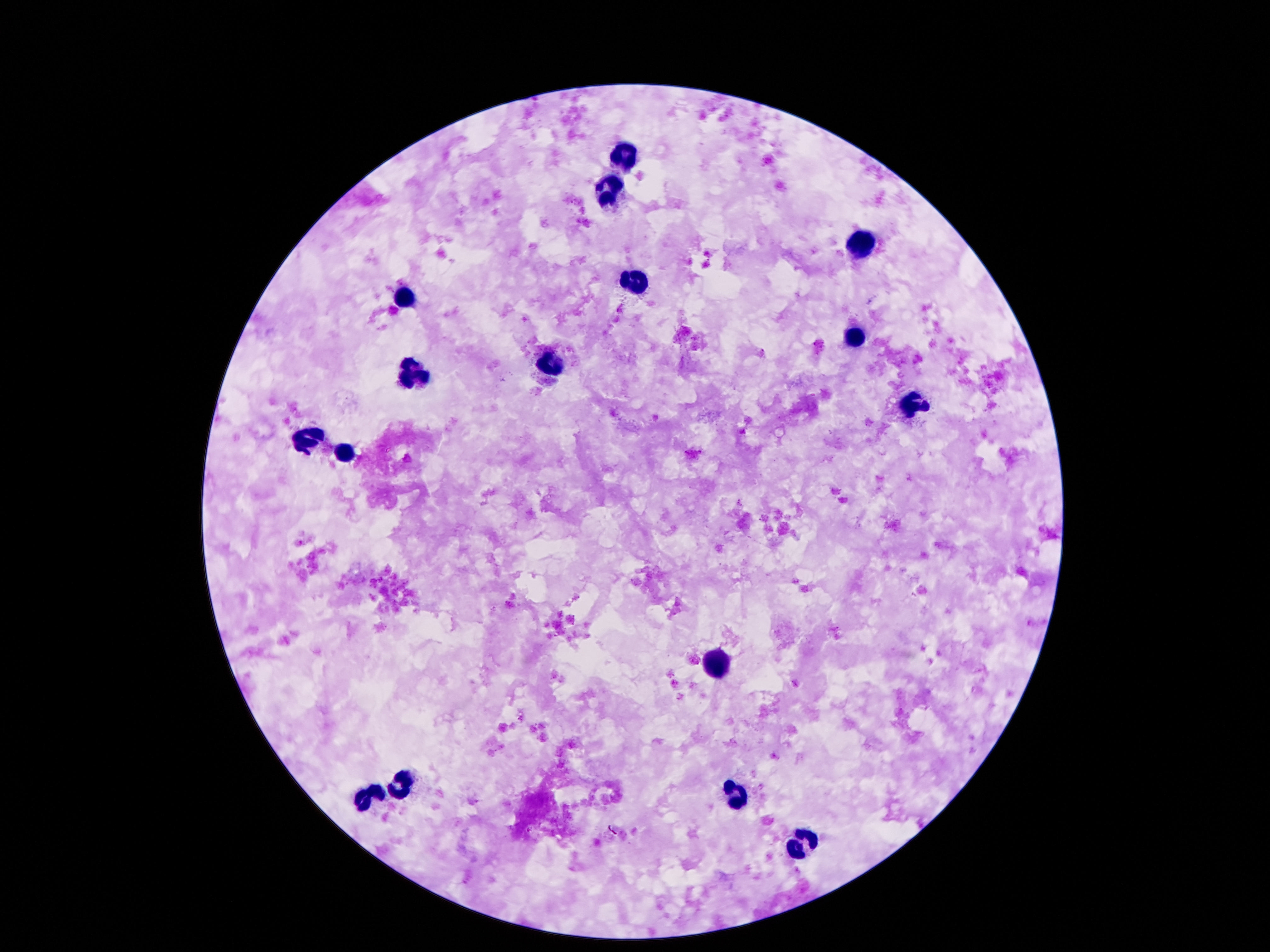
Approximate centers as (x, y) in pixels. Leukocyte locations: (622, 158), (606, 191), (864, 246), (633, 282), (400, 297), (851, 334), (547, 363), (419, 374), (910, 403), (307, 441), (347, 454), (717, 665), (402, 786), (738, 796), (368, 797), (803, 847). Giemsa-stained preparation. Patient malaria status: uninfected. Thick peripheral-blood smear. Smartphone photograph taken through the microscope eyepiece. Image is 1270×952 pixels. Single field of view. 100x magnification.